Outline each blood parasite and name the species.
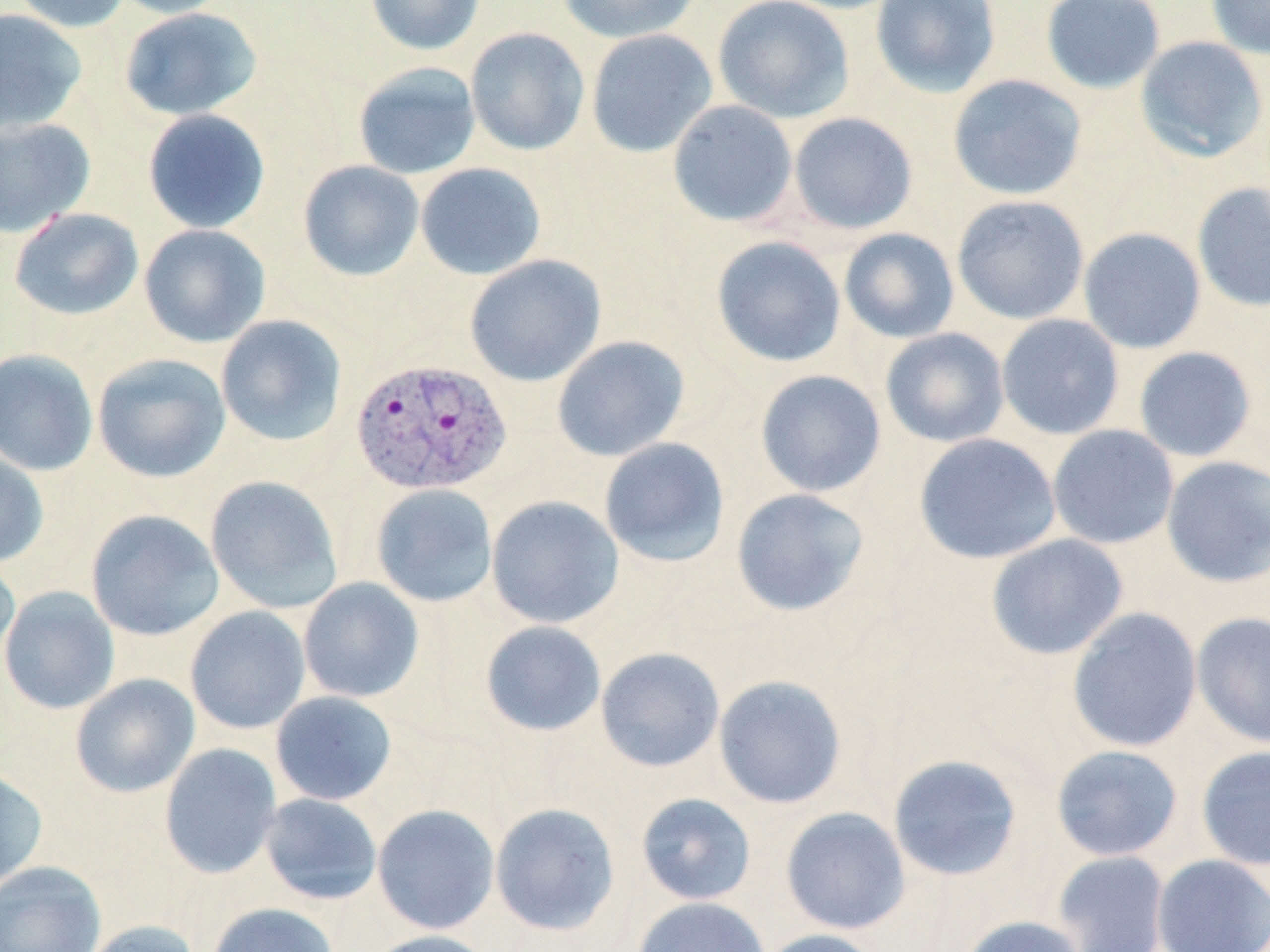

Approximate bounding boxes as [x1, y1, x2, y2] in pixels.
Plasmodium vivax-infected red blood cells: [351, 358, 512, 496].
No Plasmodium falciparum, Plasmodium ovale, Plasmodium malariae, Babesia divergens, or Trypanosoma brucei observed.

Uninfected red blood cell locations: [9, 0, 133, 33], [110, 0, 235, 19], [365, 0, 486, 56], [557, 0, 703, 44], [712, 0, 855, 123], [871, 0, 1001, 98], [1040, 0, 1165, 94], [1206, 0, 1270, 59], [119, 7, 263, 122], [0, 8, 88, 135], [464, 27, 590, 156], [586, 28, 718, 158], [1135, 36, 1269, 163], [352, 62, 481, 180], [947, 74, 1088, 201], [667, 100, 799, 228], [142, 109, 271, 234], [788, 112, 919, 235], [0, 117, 96, 238], [297, 160, 425, 282], [415, 162, 547, 281], [1191, 183, 1270, 313], [951, 195, 1089, 324], [9, 207, 144, 321], [138, 224, 271, 348], [1078, 227, 1206, 354], [839, 228, 960, 344], [710, 236, 847, 368], [464, 254, 606, 387], [996, 313, 1125, 440], [215, 314, 348, 448], [880, 327, 1010, 448], [551, 335, 691, 462], [1134, 346, 1256, 462], [0, 349, 99, 476], [92, 354, 231, 483], [754, 369, 887, 497], [1047, 424, 1180, 550], [913, 433, 1061, 564], [598, 437, 730, 567], [0, 447, 49, 567], [1161, 456, 1270, 588], [205, 475, 343, 614], [370, 483, 498, 607], [730, 488, 870, 617], [486, 495, 624, 629], [85, 509, 224, 641], [986, 534, 1129, 660], [0, 553, 20, 674], [298, 577, 425, 703], [0, 586, 120, 715], [185, 606, 311, 734], [1067, 608, 1202, 753], [1191, 612, 1270, 748], [480, 620, 607, 737], [595, 647, 725, 772], [70, 673, 200, 798], [713, 674, 848, 809], [270, 691, 397, 806], [159, 743, 282, 879], [1050, 744, 1183, 861], [1196, 745, 1270, 871], [886, 754, 1023, 882], [0, 767, 48, 891], [635, 792, 757, 906], [259, 793, 383, 904], [489, 802, 621, 937], [372, 804, 500, 935], [780, 806, 910, 935], [1051, 850, 1171, 952], [1152, 853, 1270, 952], [0, 860, 106, 952], [632, 896, 771, 952], [207, 902, 340, 952], [956, 915, 1088, 952], [81, 920, 202, 952], [757, 928, 889, 952], [361, 930, 498, 952]. Slide-level diagnosis: Plasmodium vivax. 1000x magnification. Single field of view. Thin blood film. Optical microscopy. May-Grünwald-Giemsa stain. Image is 1270×952 pixels.